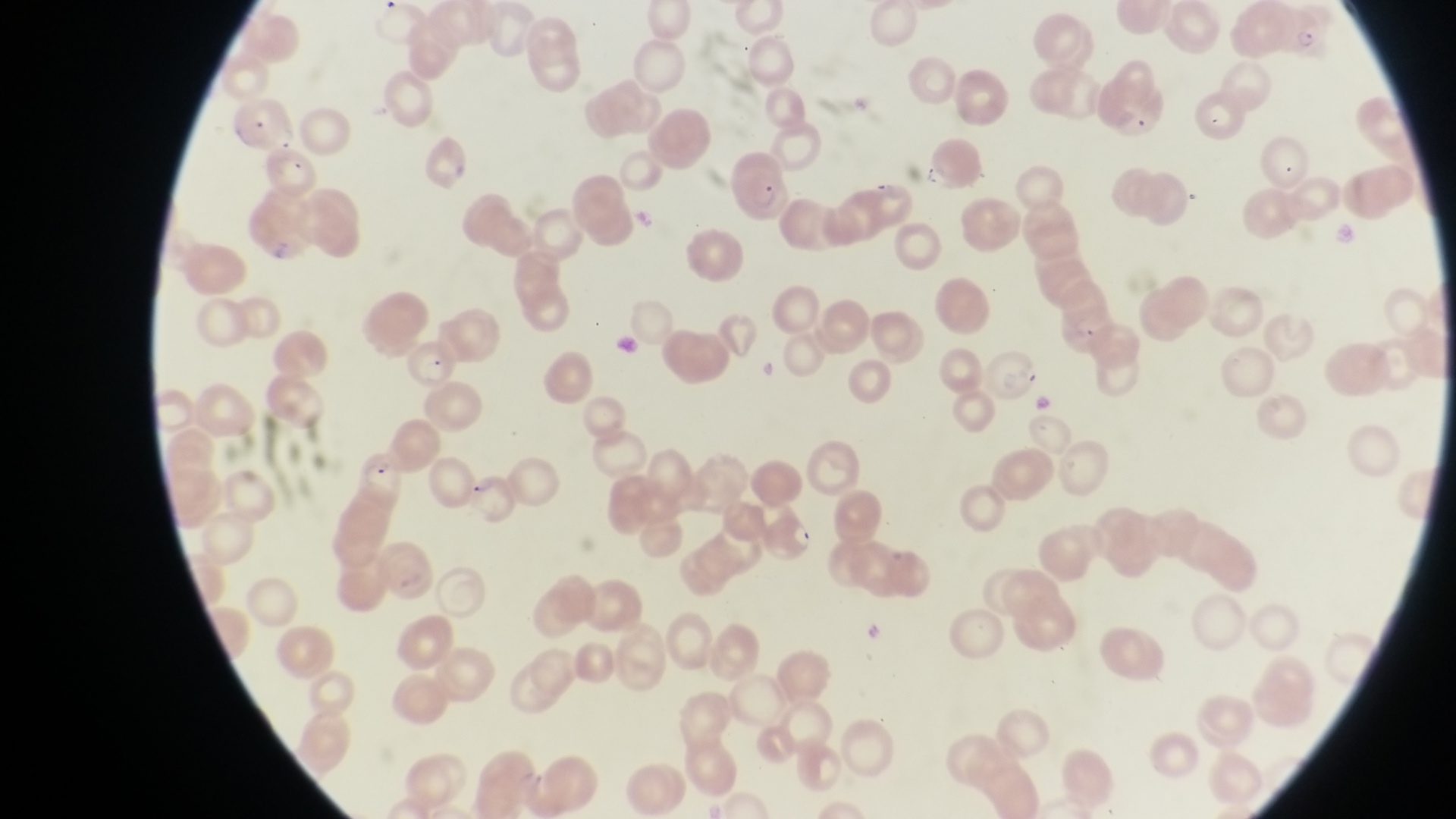
Approximate bounding boxes as {left, top, right, bottom} in pixels.
Summary:
  - Parasitised red blood cell locations: {730, 162, 793, 222}, {404, 343, 456, 386}, {359, 450, 422, 511}, {468, 467, 514, 524}
  - Trophozoite locations: {1295, 26, 1319, 56}
  - Preparation: thin blood film
  - Image size: 1456×819 pixels
  - Magnification: 1000x
  - Field of view: single
  - Country: Uganda
  - Capture: smartphone photograph through the eyepiece of an Olympus CX-23 microscope